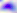
Toxoplasma gondii is seen. 400x magnification. Photomicrograph.